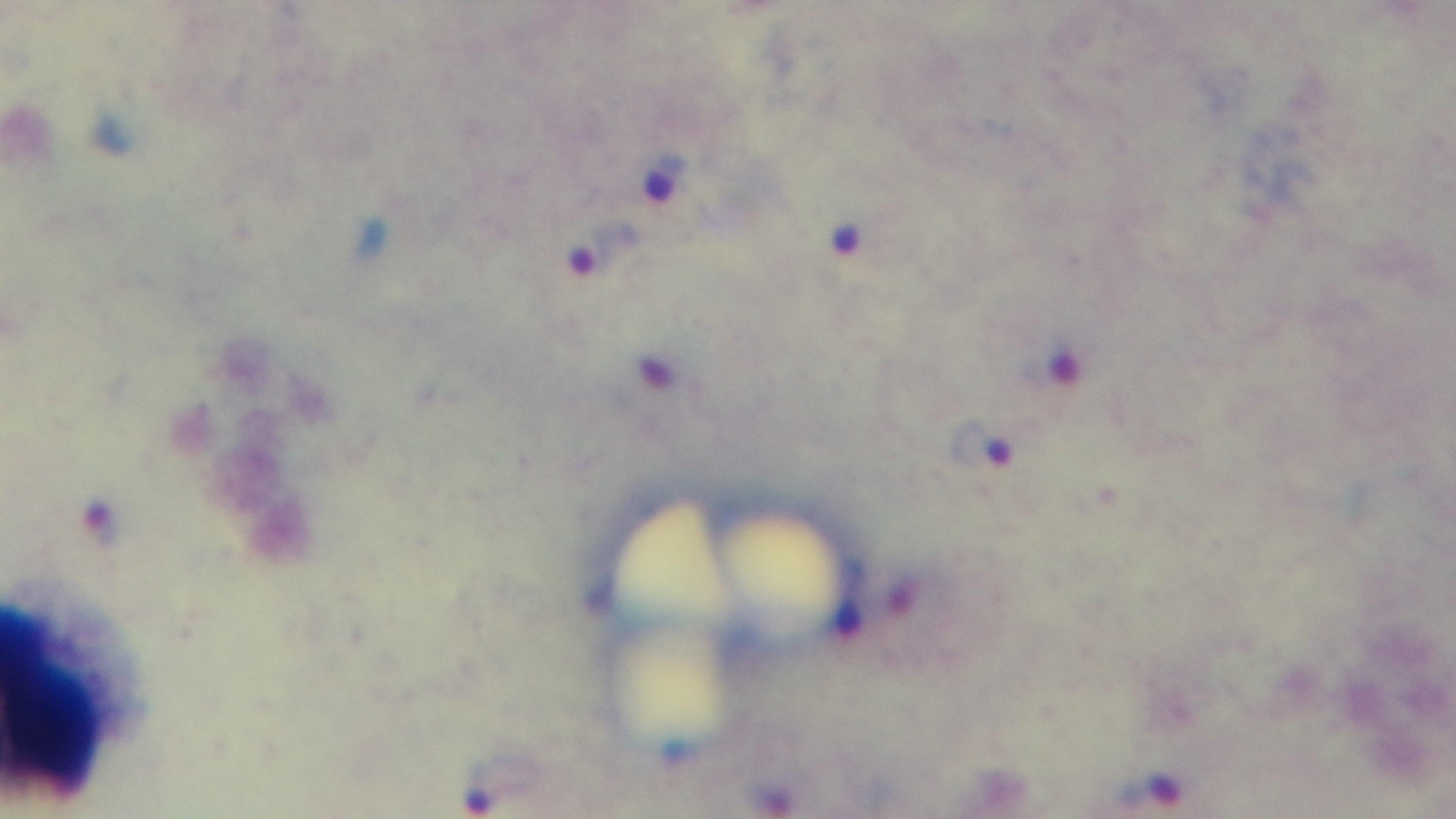
field of view = single
objective = 100x oil immersion
stain = Giemsa
malaria status = positive
capture = mounted 4K digital camera
modality = light microscopy
preparation = thick blood film